Outline each blood parasite and name the species.
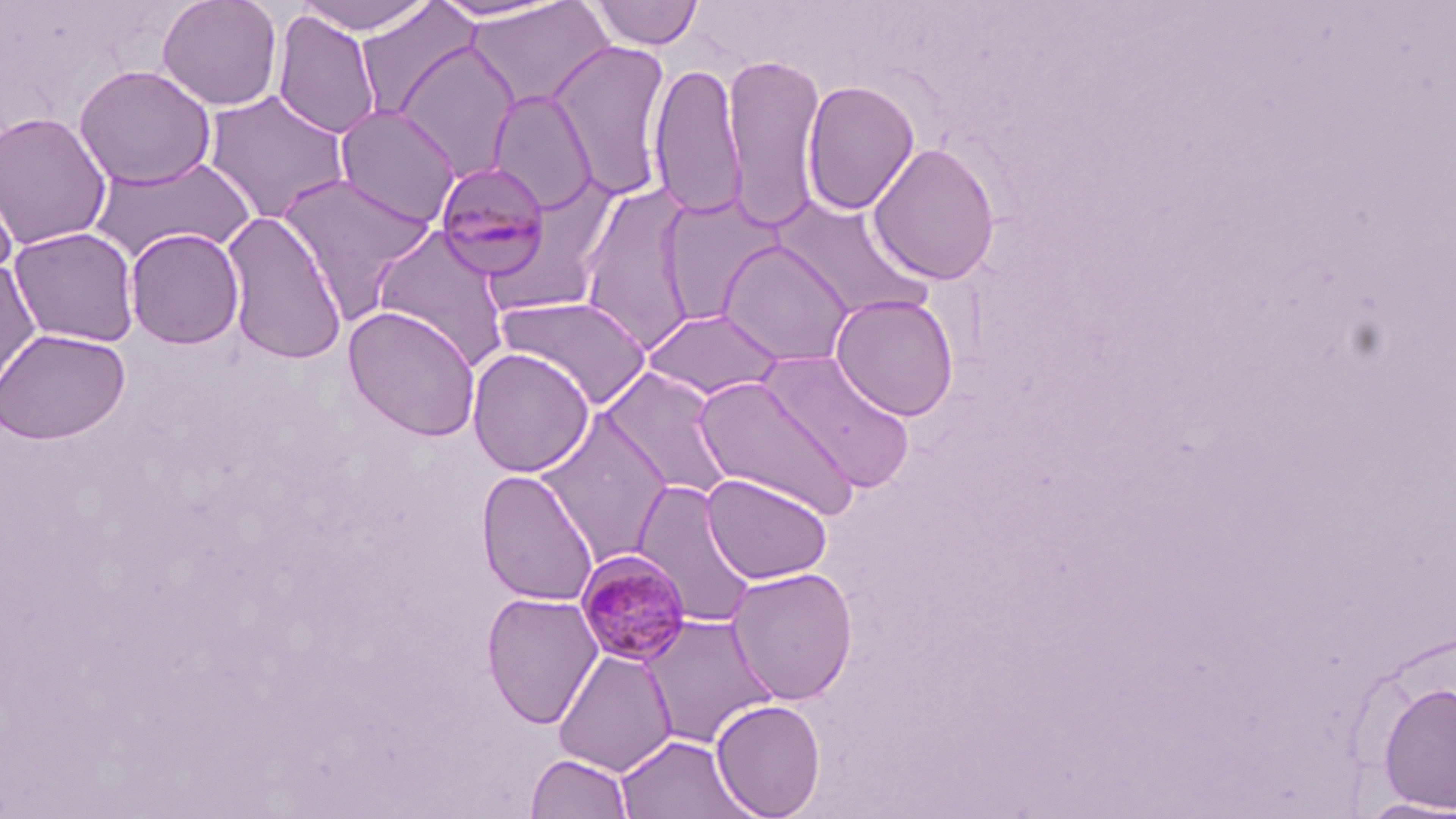
Approximate bounding boxes as (x1, y1, x2, y2) in pixels.
Plasmodium malariae-infected red blood cells: (435, 161, 552, 280), (575, 550, 693, 667).
No Plasmodium falciparum, Plasmodium ovale, Plasmodium vivax, Babesia divergens, or Trypanosoma brucei observed.

Summary:
  - Uninfected red blood cell locations: (156, 0, 284, 112), (292, 0, 440, 36), (426, 0, 574, 24), (588, 0, 704, 51), (463, 1, 615, 112), (356, 3, 479, 123), (272, 9, 382, 140), (393, 40, 521, 180), (547, 41, 672, 199), (723, 52, 826, 230), (648, 61, 747, 220), (73, 64, 217, 190), (801, 79, 921, 216), (487, 89, 598, 214), (203, 90, 351, 225), (333, 105, 462, 227), (0, 111, 113, 250), (867, 141, 1001, 285), (86, 154, 256, 264), (0, 163, 19, 283), (275, 172, 438, 318), (577, 181, 700, 355), (657, 194, 783, 327), (772, 196, 933, 323), (220, 210, 348, 365), (369, 225, 513, 371), (8, 226, 141, 347), (124, 227, 245, 350), (718, 239, 856, 368), (0, 259, 41, 397), (829, 292, 960, 421), (496, 294, 652, 410), (343, 305, 482, 441), (643, 308, 785, 401), (0, 328, 130, 445), (466, 347, 595, 477), (762, 351, 916, 494), (598, 367, 735, 502), (693, 376, 860, 520), (534, 411, 674, 566), (476, 468, 599, 607), (700, 473, 833, 584), (631, 479, 762, 630), (725, 566, 859, 705), (480, 591, 604, 729), (638, 614, 778, 749), (553, 649, 678, 777), (1377, 681, 1456, 813), (710, 699, 826, 818), (615, 733, 752, 818), (525, 752, 634, 819), (1352, 796, 1456, 819)
  - Slide-level diagnosis: Plasmodium malariae
  - Modality: optical microscopy
  - Image size: 1456×819 pixels
  - Preparation: thin blood film
  - Stain: May-Grünwald-Giemsa
  - Field of view: single
  - Magnification: 1000x